Classify this cell by malaria status.
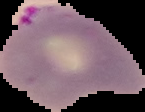

Parasitized.

Summary:
  - Image size: 145×112 pixels
  - Preparation: thin blood film
  - Image type: segmented cell region with the area outside set to black